Give the extent of all Plasmodium falciparum-infected red blood cells.
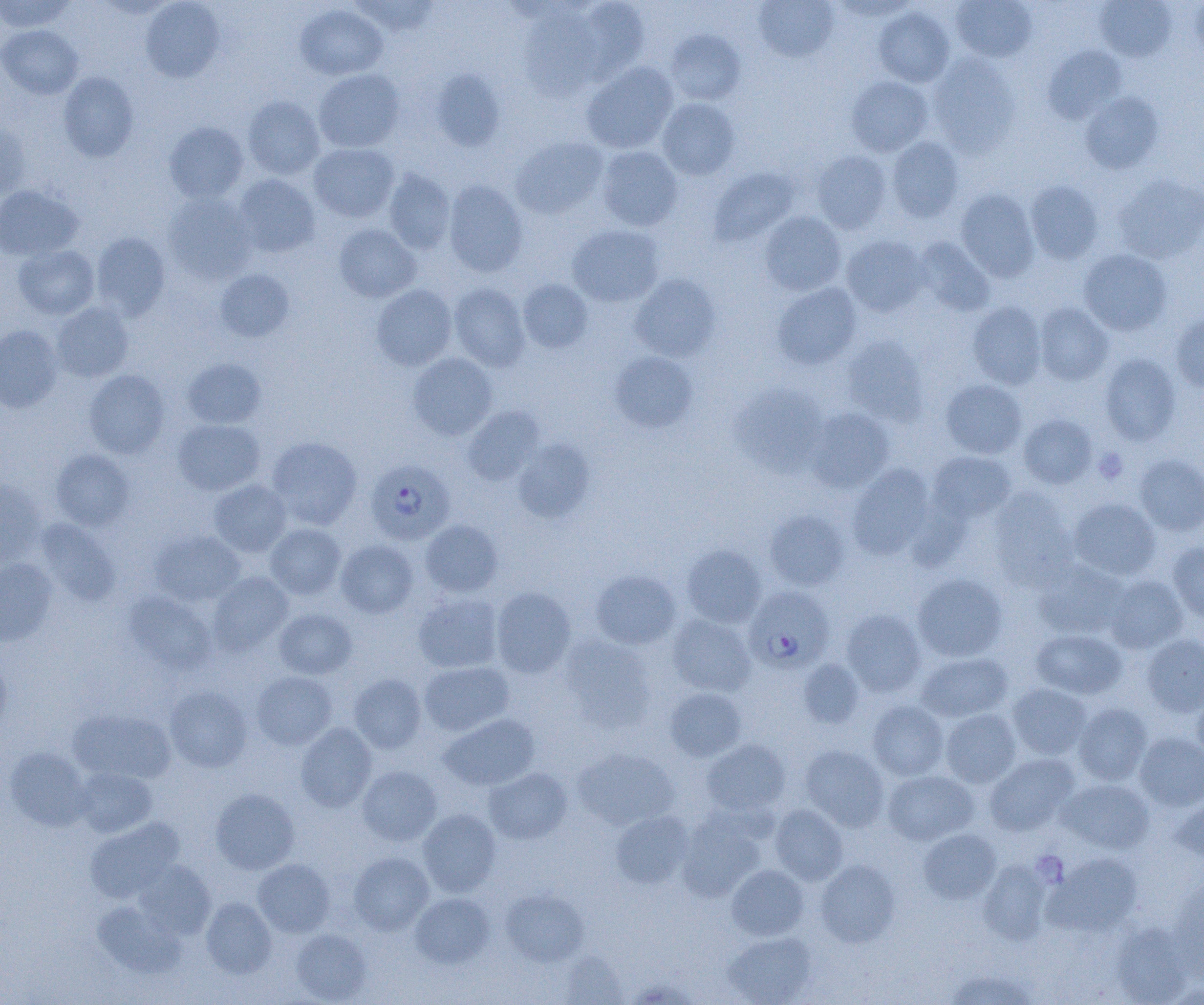
Approximate bounding boxes as (x1,y1)-(x2,y2) corner pairs in pixels.
Plasmodium falciparum-infected red blood cells: (365,459)-(455,545), (743,587)-(833,673).

Summary:
  - Uninfected red blood cell locations: (0,0)-(77,33), (141,0)-(224,83), (349,0)-(440,37), (576,0)-(650,82), (753,0)-(838,63), (830,0)-(920,20), (951,0)-(1037,63), (1190,0)-(1204,58), (1094,1)-(1177,62), (295,4)-(388,80), (518,7)-(604,101), (874,7)-(955,87), (0,25)-(83,99), (666,30)-(746,105), (1043,46)-(1126,124), (928,54)-(1020,156), (582,61)-(678,154), (430,68)-(505,151), (313,69)-(405,153), (58,72)-(139,161), (845,76)-(933,157), (1079,91)-(1164,174), (243,96)-(325,179), (658,98)-(741,180), (0,122)-(30,200), (163,122)-(248,203), (888,136)-(964,222), (511,137)-(608,219), (309,143)-(398,222), (597,146)-(683,231), (811,150)-(892,234), (708,167)-(799,247), (383,168)-(455,254), (232,174)-(320,258), (1112,174)-(1204,264), (443,180)-(528,277), (1025,180)-(1103,264), (0,185)-(83,260), (955,189)-(1040,282), (163,193)-(257,284), (759,211)-(846,296), (333,224)-(421,302), (567,225)-(664,307), (91,232)-(170,320), (842,235)-(929,317), (913,237)-(994,315), (13,244)-(99,320), (1078,249)-(1172,336), (215,268)-(295,342), (629,273)-(721,361), (518,279)-(593,354), (772,282)-(862,370), (448,283)-(530,371), (371,285)-(457,371), (967,301)-(1047,389), (51,302)-(134,382), (1034,302)-(1113,385), (1170,313)-(1204,392), (0,324)-(63,413), (841,335)-(928,426), (610,352)-(697,433), (408,353)-(497,440), (1100,353)-(1181,446), (182,357)-(267,428), (84,370)-(170,458), (941,379)-(1027,459), (731,383)-(829,477), (462,406)-(545,486), (806,408)-(895,493), (1019,414)-(1097,489), (172,419)-(265,495), (266,436)-(362,530), (513,439)-(593,522), (51,449)-(135,530), (928,451)-(1015,525), (1135,454)-(1204,535), (846,465)-(934,560), (208,479)-(291,557), (0,480)-(46,566), (987,487)-(1078,590), (1068,498)-(1161,580), (764,510)-(849,590), (35,519)-(119,606), (420,519)-(503,597), (265,523)-(346,600), (150,530)-(245,607), (335,540)-(418,618), (1167,542)-(1204,623), (681,544)-(766,628), (0,558)-(57,647), (1034,561)-(1130,639), (590,570)-(681,650), (207,572)-(293,656), (912,573)-(1008,662), (1104,575)-(1189,654), (491,587)-(576,678), (123,591)-(216,675), (413,592)-(502,673), (274,608)-(357,679), (841,608)-(927,697), (667,615)-(756,696), (1030,628)-(1127,700), (1141,634)-(1204,717), (560,635)-(657,732), (916,652)-(1013,723), (0,655)-(12,735), (798,659)-(864,729), (418,661)-(513,736), (252,671)-(337,749), (349,674)-(426,753), (1008,683)-(1092,759), (165,685)-(252,772), (1190,687)-(1204,764), (665,688)-(746,761), (867,701)-(949,780), (1073,703)-(1152,786), (69,708)-(175,783), (940,709)-(1021,788), (439,714)-(539,790), (295,723)-(377,811), (1135,732)-(1204,811), (702,739)-(790,816), (800,745)-(890,831), (4,747)-(91,831), (573,748)-(679,830), (984,753)-(1079,836), (74,766)-(157,838), (357,766)-(442,846), (484,767)-(572,845), (883,770)-(978,845), (1059,778)-(1154,853), (210,788)-(299,874), (1170,797)-(1204,863), (770,804)-(848,884), (677,808)-(766,902), (418,809)-(501,897), (610,811)-(693,888), (84,817)-(184,903), (918,829)-(1001,904), (348,851)-(434,935), (1044,852)-(1143,936), (253,859)-(335,937), (979,859)-(1052,944), (815,860)-(900,947), (135,861)-(215,939), (727,864)-(809,940), (1170,875)-(1204,977), (500,888)-(589,967), (410,892)-(494,969), (201,897)-(277,978), (93,901)-(185,978), (1109,922)-(1193,1005), (291,929)-(371,1003), (723,931)-(817,1005), (559,952)-(627,1004), (945,969)-(1039,1005)
  - Platelet locations: (1093,447)-(1128,484)
  - Slide-level diagnosis: Plasmodium falciparum
  - Modality: optical microscopy
  - Preparation: thin blood film
  - Magnification: 1000x
  - Image size: 1204×1005 pixels
  - Field of view: single